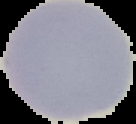
Summary:
  - Image size: 136×124 pixels
  - Preparation: thin blood smear
  - Malaria status: uninfected
  - Image type: cell region segmented out of the field of view; surrounding area masked to black